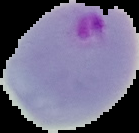

image size = 139×133 pixels
image type = cell region segmented out of the field of view; surrounding area masked to black
preparation = thin blood film
malaria status = parasitized